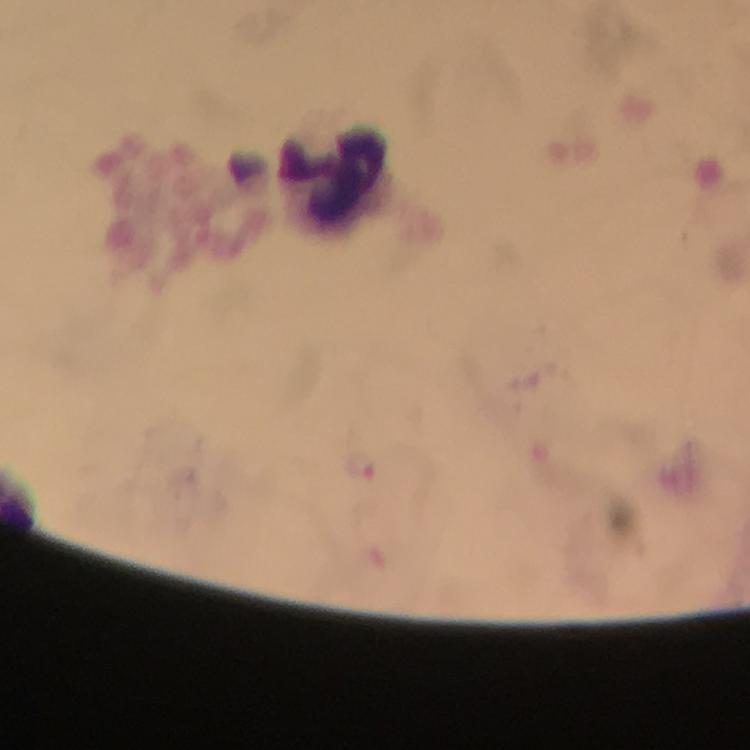

Approximate object centers, in pixels from the top-left corner. Leukocyte locations: (x=334, y=176). Malaria parasites: none seen. A crop from one field of view. Image is 750×750 pixels. Thick smear. 100x magnification. Immersion oil applied. From a diagnostic examination for malaria. Giemsa-stained preparation. Photographed with a smartphone mounted on the microscope.